State which parasite is depicted.
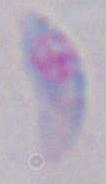

This is Toxoplasma gondii.

Captured at 1000x magnification. Photomicrograph.